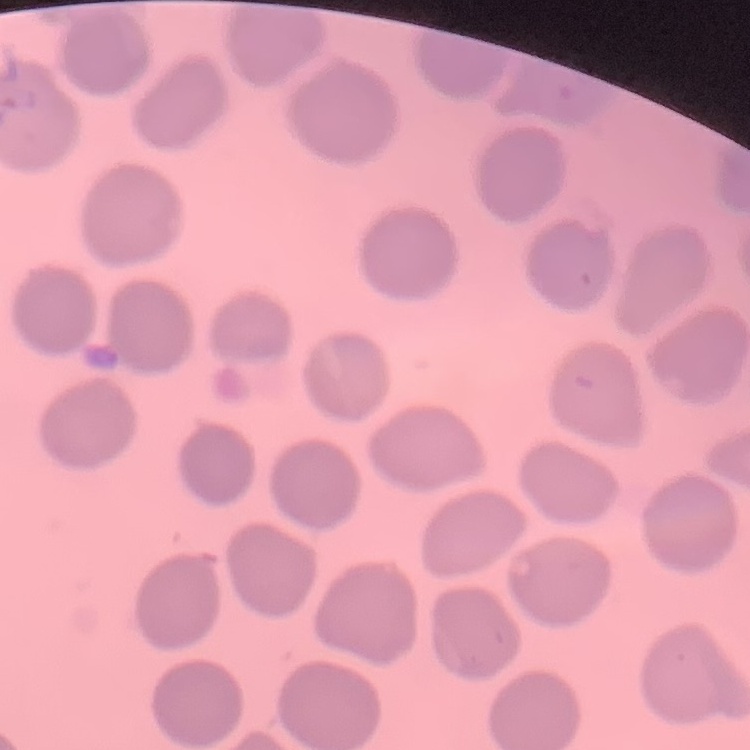
Summary:
  - Erythrocyte morphology: no rouleaux formation
  - Image type: square crop of a larger photomicrograph
  - Preparation: thin peripheral smear
  - Stain: Field's or Giemsa